State the preparation type.
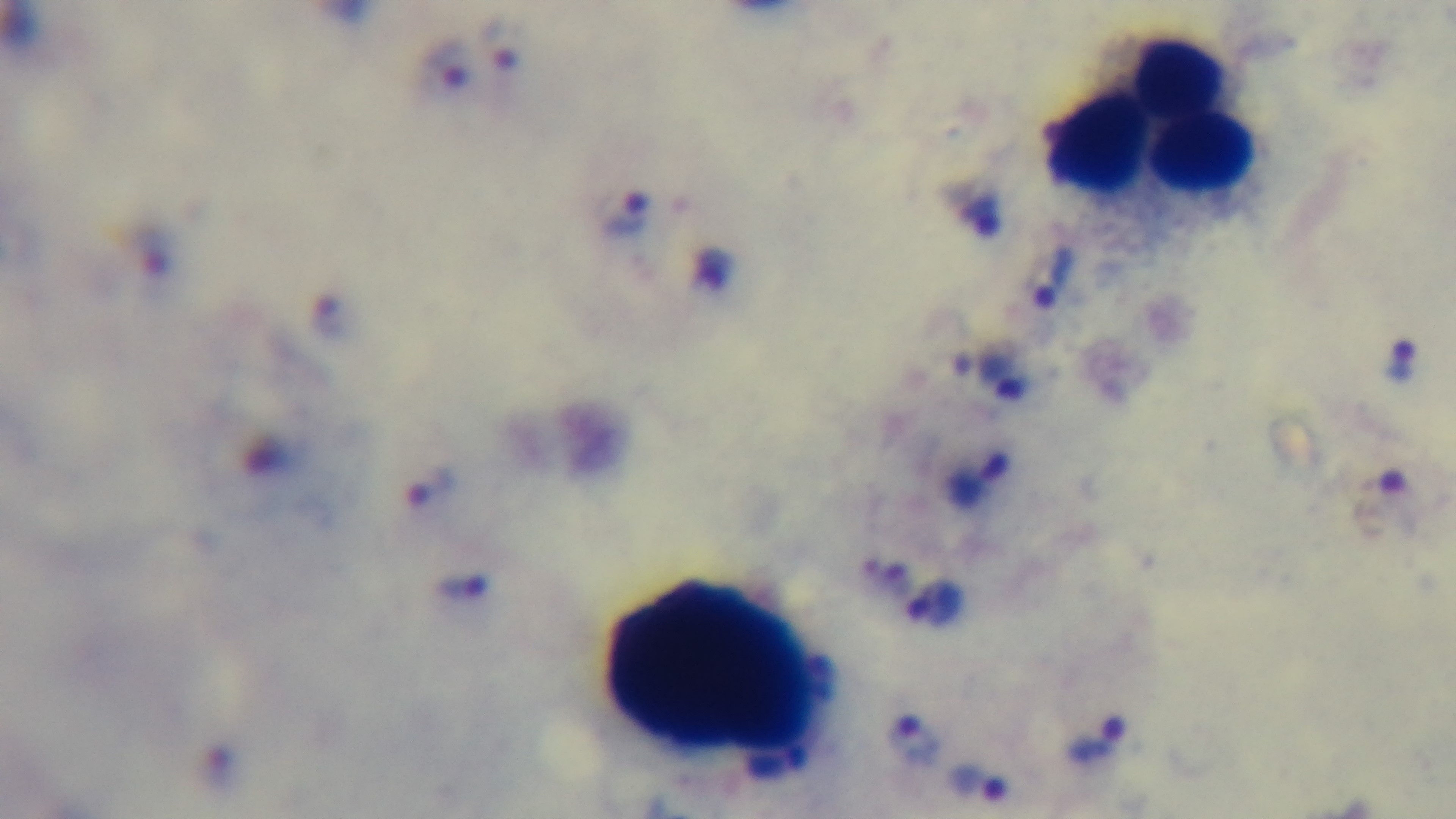

Thick.

Malaria status: infected. Giemsa-stained. Light microscopy. 100x oil-immersion objective. One field from the slide. Captured with a mounted 4K digital camera.